Locate every blood parasite and identify its species.
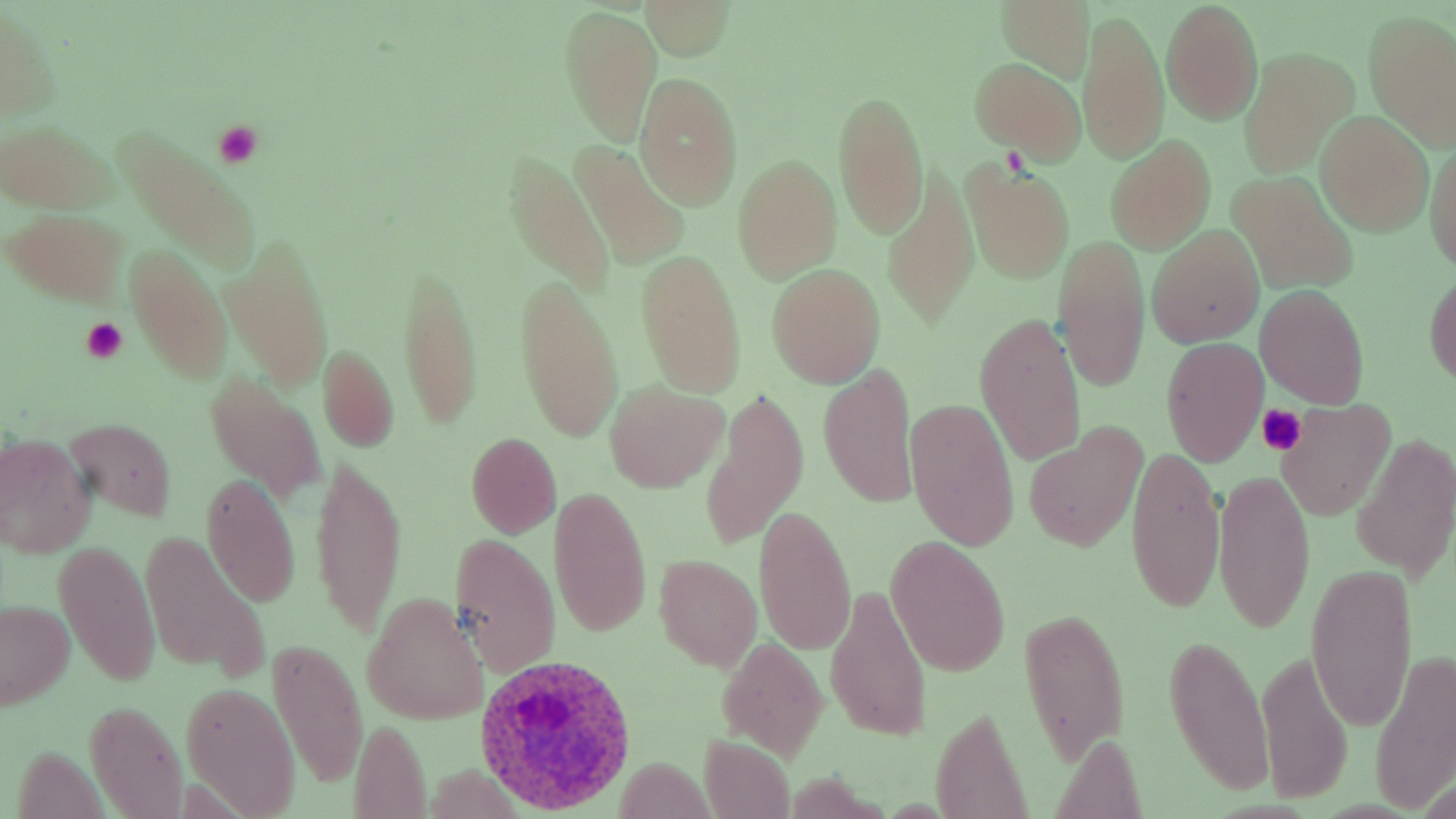

Approximate bounding boxes as [x1, y1, x2, y2] in pixels.
Plasmodium ovale-infected red blood cells: [473, 654, 638, 815].
No Plasmodium falciparum, Plasmodium malariae, Plasmodium vivax, Babesia divergens, or Trypanosoma brucei observed.

Uninfected red blood cell locations: [643, 1, 733, 60], [996, 2, 1095, 82], [1161, 2, 1263, 123], [561, 4, 659, 145], [0, 5, 58, 125], [1078, 11, 1169, 165], [1363, 11, 1456, 151], [1239, 48, 1356, 177], [969, 59, 1086, 160], [634, 73, 744, 208], [833, 90, 929, 239], [1316, 112, 1432, 234], [2, 121, 113, 214], [112, 127, 264, 271], [1425, 130, 1456, 275], [1105, 136, 1217, 253], [572, 141, 687, 268], [503, 155, 613, 295], [732, 155, 841, 282], [962, 161, 1075, 283], [882, 166, 976, 329], [1229, 172, 1357, 293], [5, 207, 130, 308], [1147, 225, 1264, 347], [1051, 234, 1150, 392], [222, 237, 333, 387], [123, 242, 232, 385], [636, 250, 748, 397], [396, 260, 483, 429], [768, 264, 886, 386], [1425, 272, 1456, 386], [514, 273, 624, 444], [1256, 285, 1369, 407], [974, 312, 1087, 468], [1160, 337, 1268, 466], [317, 345, 399, 453], [818, 364, 920, 509], [205, 373, 325, 501], [604, 380, 726, 491], [700, 390, 807, 548], [906, 398, 1020, 551], [1277, 399, 1396, 520], [64, 418, 176, 521], [1023, 426, 1147, 550], [0, 433, 95, 557], [465, 433, 562, 537], [1352, 435, 1454, 581], [1125, 443, 1225, 617], [311, 456, 407, 640], [1212, 469, 1315, 632], [202, 473, 301, 606], [548, 487, 652, 638], [755, 506, 857, 655], [449, 531, 561, 676], [143, 534, 270, 678], [53, 537, 162, 689], [886, 538, 1011, 676], [654, 555, 762, 671], [1305, 563, 1419, 732], [827, 583, 931, 741], [362, 593, 488, 726], [0, 599, 76, 710], [1017, 605, 1130, 764], [1161, 633, 1275, 800], [269, 636, 366, 789], [717, 638, 827, 759], [1370, 645, 1456, 811], [1255, 646, 1352, 805], [181, 682, 300, 816], [85, 698, 187, 818], [929, 705, 1032, 819], [349, 719, 432, 818], [1050, 733, 1149, 818], [699, 735, 795, 818], [612, 758, 717, 815]. Platelet locations: [212, 121, 262, 167], [80, 316, 129, 362], [1255, 403, 1308, 456]. Slide-level diagnosis: Plasmodium ovale. Thin blood film. Single field of view. Light microscopy. Image is 1456×819 pixels. May-Grünwald-Giemsa-stained preparation. Captured at 1000x magnification.